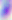

Toxoplasma gondii is shown. 400x magnification. Photomicrograph.